Outline each blood parasite and name the species.
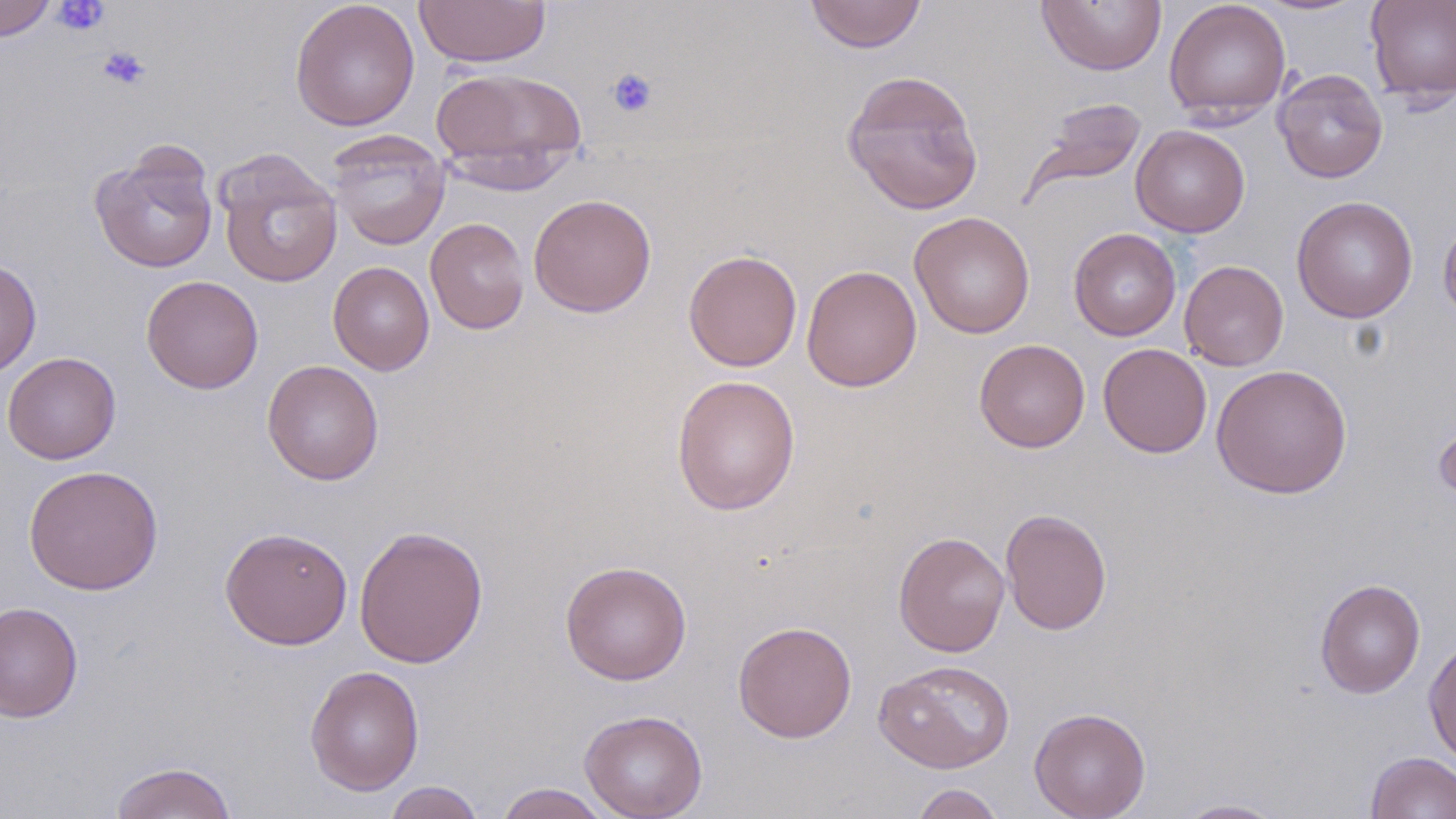

No blood parasites seen.

slide-level diagnosis = no evidence of blood parasites
field of view = single
image size = 1456×819 pixels
uninfected red blood cell locations = approximate bounding boxes as (x1,y1)-(x2,y2) corner pairs in pixels: (0,0)-(55,41), (289,0)-(420,131), (413,0)-(551,68), (804,0)-(927,53), (1163,0)-(1291,124), (1365,0)-(1456,106), (1035,1)-(1167,76), (430,66)-(589,184), (1273,69)-(1388,183), (841,70)-(984,215), (1024,96)-(1147,198), (1131,125)-(1250,237), (327,131)-(450,251), (89,143)-(219,274), (214,148)-(343,289), (528,194)-(657,317), (1291,195)-(1418,323), (909,211)-(1035,339), (1439,213)-(1456,325), (425,217)-(530,335), (1069,228)-(1181,341), (683,250)-(802,371), (0,258)-(41,378), (1179,260)-(1289,371), (328,261)-(435,375), (802,264)-(922,393), (141,275)-(264,394), (974,339)-(1090,453), (1098,342)-(1213,458), (2,351)-(121,464), (262,359)-(384,485), (1211,364)-(1352,499), (671,374)-(801,516), (1433,414)-(1456,509), (23,464)-(164,595), (1001,508)-(1112,636), (353,524)-(489,668), (219,526)-(354,650), (893,531)-(1010,657), (560,559)-(692,686), (1314,578)-(1426,698), (0,601)-(84,723), (732,620)-(857,743), (1423,637)-(1456,768), (873,659)-(1015,773), (304,665)-(425,795), (1029,707)-(1151,819), (579,709)-(709,819), (1365,751)-(1456,818), (109,761)-(238,819), (383,781)-(486,819), (493,783)-(613,818), (910,783)-(1007,819), (1173,798)-(1288,818)
magnification = 1000x
platelet locations = approximate bounding boxes as (x1,y1)-(x2,y2) corner pairs in pixels: (52,1)-(110,35), (97,46)-(151,92), (606,67)-(658,119)
preparation = thin blood smear
stain = May-Grünwald-Giemsa
modality = optical microscopy